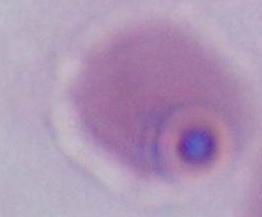

{
  "modality": "photomicrograph",
  "identification": "Plasmodium",
  "magnification": "400x or 1000x"
}